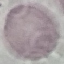

Summary:
  - Malaria status: uninfected
  - Stain: Giemsa
  - Capture: smartphone through the microscope eyepiece
  - Preparation: thin blood smear
  - Image type: automatically extracted cell patch, resized to 64 × 64 pixels